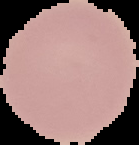 Segmented cell region on a black background. Malaria status: uninfected. Image is 139×145 pixels. From a thin blood smear.